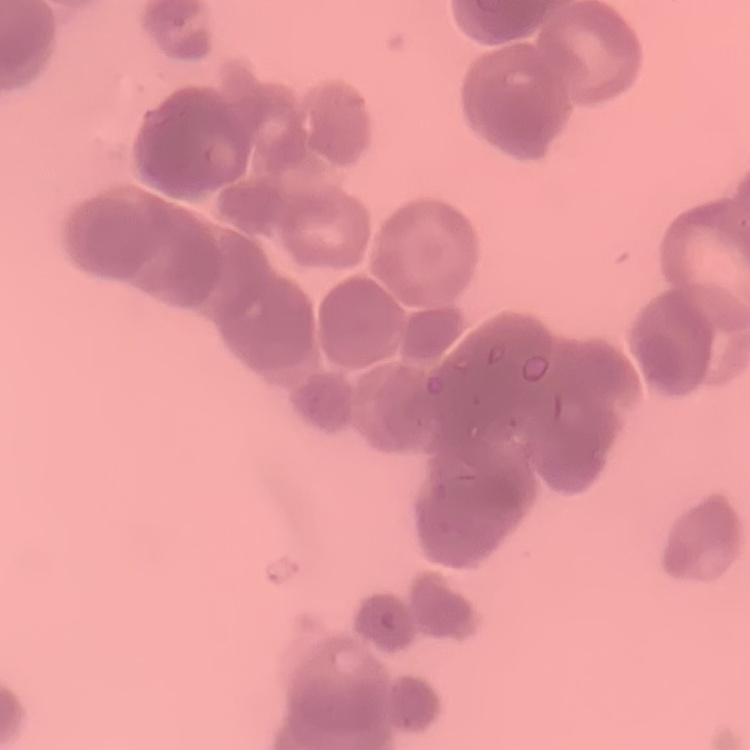
The erythrocytes exhibit rouleaux formation. Thin peripheral smear. One tile cut from a larger photomicrograph. Stained with either Field's or Giemsa.